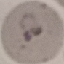
{
  "malaria_status": "parasitized",
  "stain": "Giemsa",
  "preparation": "thin blood smear",
  "image_type": "automatically extracted cell patch, resized to 64 × 64 pixels",
  "capture": "smartphone camera at the microscope eyepiece"
}